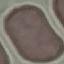
Summary:
  - Result: no malaria parasites detected
  - Capture: smartphone through the microscope eyepiece
  - Image type: cell patch, automatically extracted from a larger field of view and resized to 64 × 64 pixels
  - Preparation: thin blood film
  - Stain: Giemsa